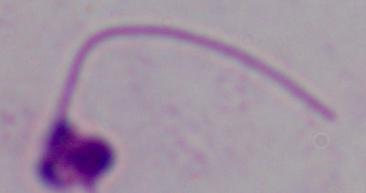
A Leishmania parasite is seen. 1000x magnification. Photomicrograph.